State the preparation type.
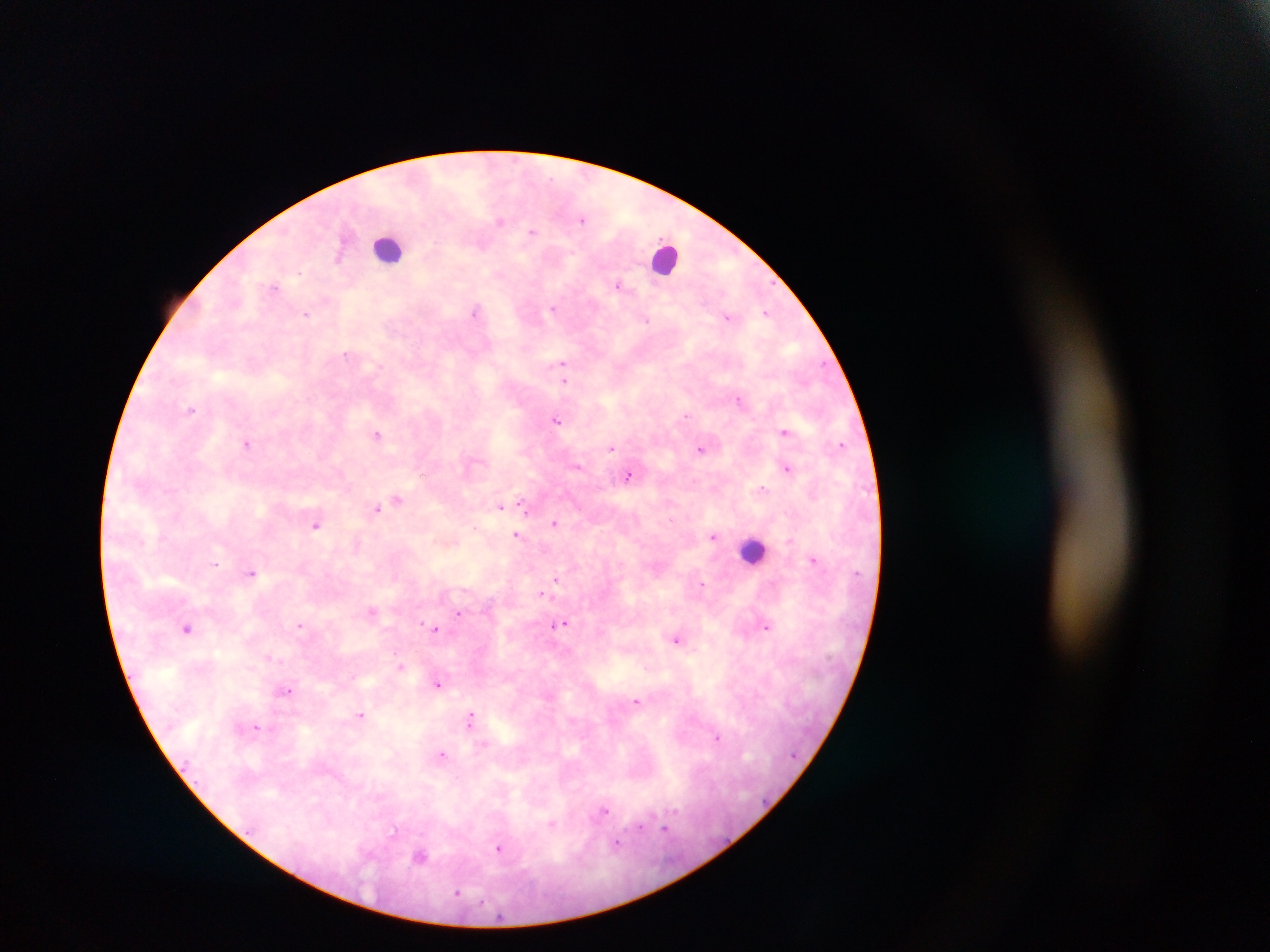

This is a thick smear.

Approximate centers as {x, y} in pixels.
Summary:
  - Leukocyte locations: {389, 248}, {667, 258}, {755, 550}
  - Plasmodium parasite locations: {583, 219}, {500, 221}, {532, 231}, {481, 246}, {338, 257}, {618, 285}, {275, 286}, {553, 308}, {475, 311}, {766, 312}, {307, 314}, {727, 317}, {646, 320}, {346, 353}, {562, 364}, {564, 380}, {738, 400}, {191, 410}, {685, 416}, {555, 420}, {785, 432}, {376, 434}, {247, 443}, {841, 445}, {611, 448}, {701, 449}, {577, 466}, {787, 468}, {422, 475}, {628, 476}, {762, 488}, {397, 500}, {500, 506}, {524, 507}, {377, 509}, {554, 523}, {315, 526}, {474, 526}, {516, 535}, {712, 537}, {813, 560}, {215, 564}, {251, 573}, {555, 578}, {702, 585}, {542, 594}, {371, 611}, {458, 613}, {422, 623}, {562, 624}, {300, 625}, {766, 626}, {188, 628}, {436, 629}, {676, 639}, {269, 657}, {397, 658}, {400, 666}, {438, 684}, {286, 691}, {637, 701}, {361, 715}, {470, 719}, {256, 727}, {716, 737}, {442, 754}, {604, 811}, {551, 823}, {640, 827}, {665, 828}, {393, 833}, {616, 844}, {499, 849}, {420, 855}, {457, 893}
  - Country: Ghana
  - Field of view: single
  - Image size: 1270×952 pixels
  - Capture: mobile-phone photograph through a microscope